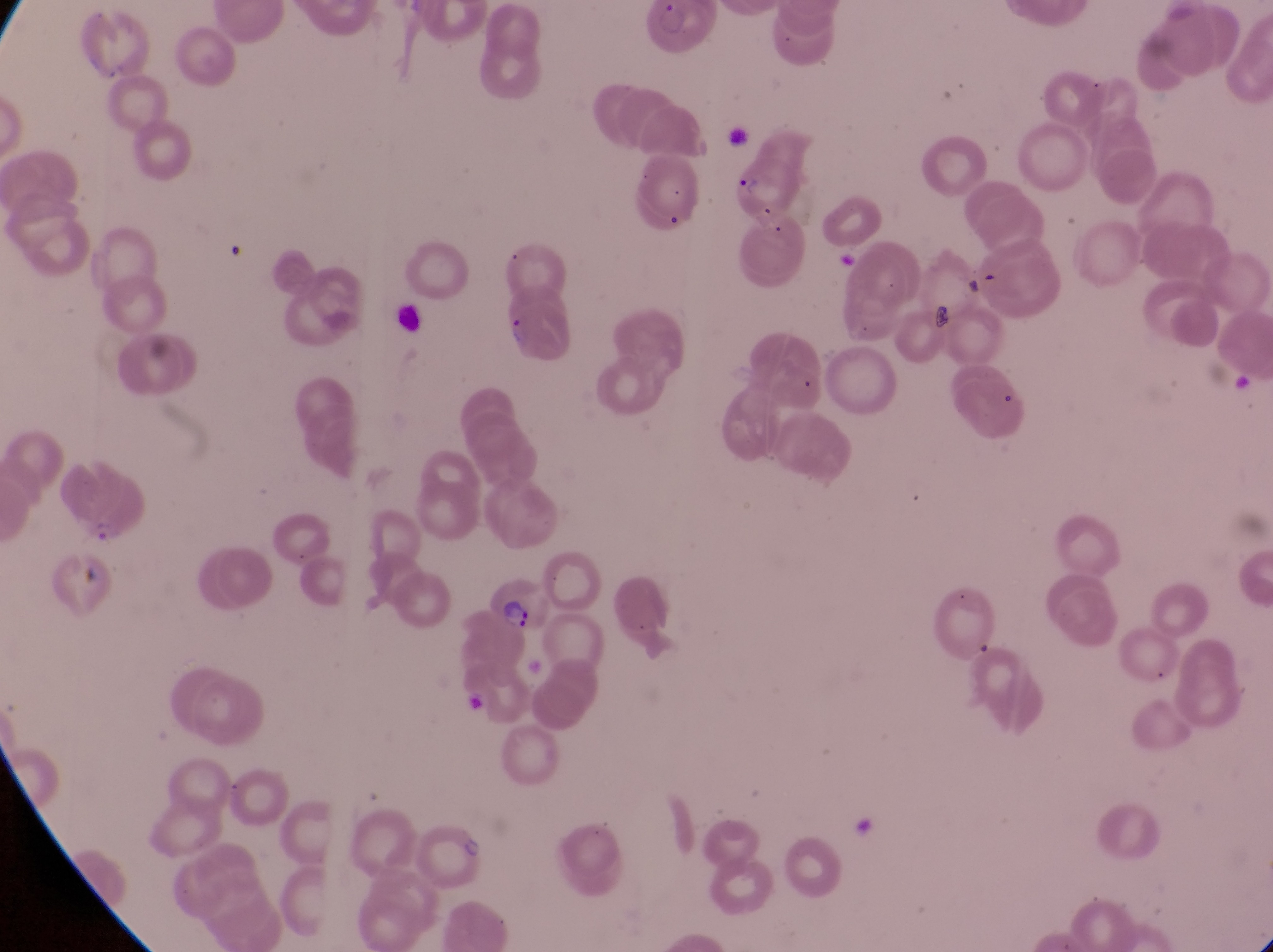
parasitised red blood cell locations = approximate bounding boxes as [left, top, right, bottom] in pixels: [724, 150, 806, 220], [60, 477, 143, 543], [487, 572, 550, 634]
image size = 1273×952 pixels
magnification = 1000x
capture = smartphone photograph through the eyepiece of an Olympus CX-23 microscope
field of view = single
country = Uganda
artifact (platelet-like body, stain precipitate, or debris) locations = approximate bounding boxes as [left, top, right, bottom] in pixels: [921, 297, 961, 342]
preparation = thin blood film